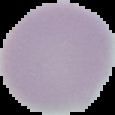
Malaria status: uninfected. From a thin blood film. Segmented cell region on a black background. Image is 115×115 pixels.